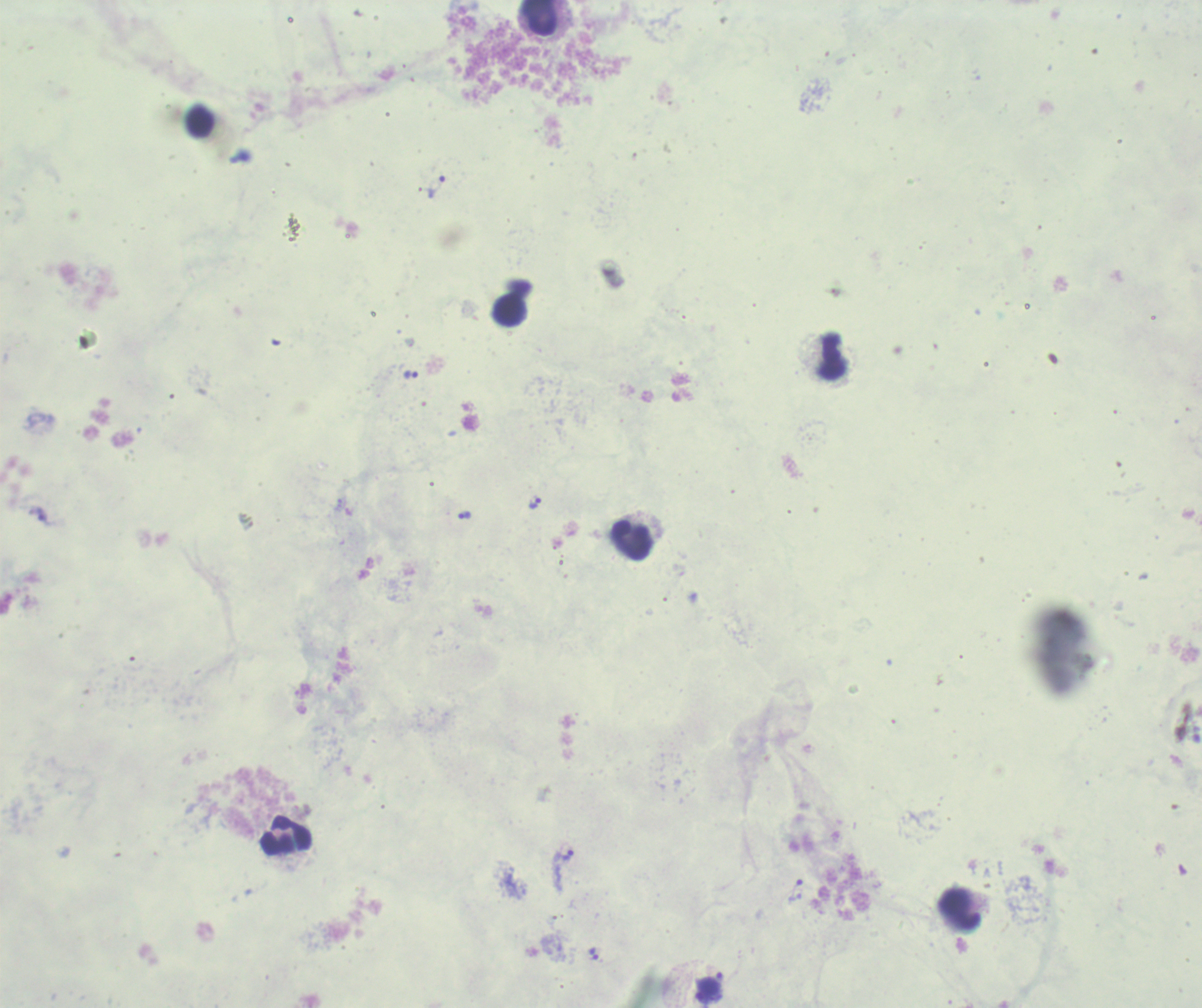

{
  "stain": "Romanowsky",
  "background_quality": "unsatisfactory",
  "context": "previously used in an actual diagnosis",
  "image_size": "1202×1008 pixels",
  "leukocyte_locations": "approximate object centers, in pixels from the top-left corner: (x=539, y=17), (x=200, y=124), (x=510, y=311), (x=833, y=356), (x=631, y=542), (x=285, y=836), (x=959, y=910)",
  "result": "malaria parasites identified",
  "trophozoite_locations": "approximate object centers, in pixels from the top-left corner: (x=436, y=186), (x=410, y=376), (x=534, y=503), (x=463, y=514), (x=41, y=518), (x=567, y=855), (x=795, y=891), (x=593, y=955)",
  "preparation": "thick blood smear",
  "field_of_view": "one from this slide",
  "magnification": "100x"
}